Classify this cell by malaria status.
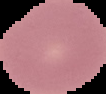
Uninfected.

Summary:
  - Image size: 106×94 pixels
  - Preparation: thin blood smear
  - Image type: segmented cell region on a black background